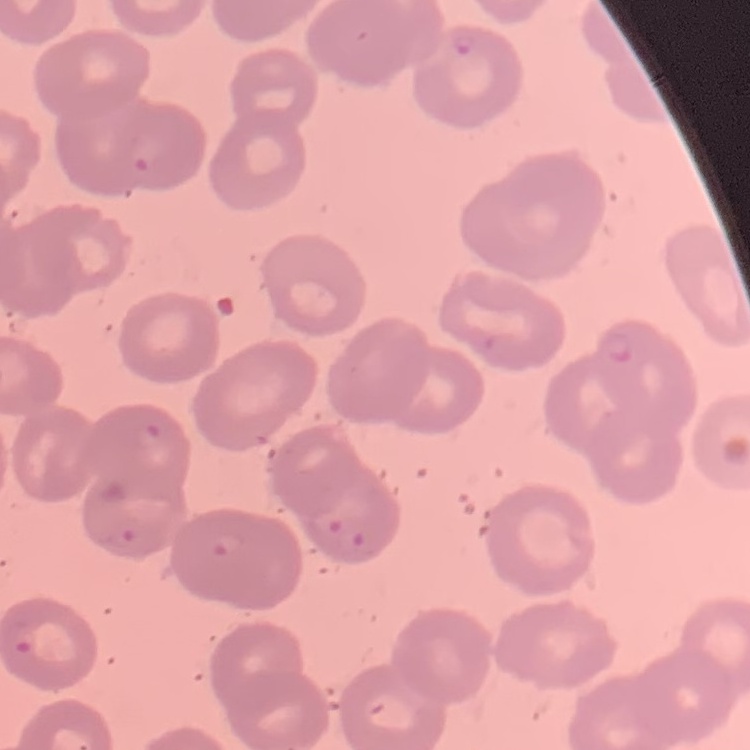

red blood cell morphology = no rouleaux formation
image type = square crop of a larger photomicrograph
stain = Field's or Giemsa
preparation = thin blood film